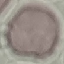

Malaria status: uninfected. Cell patch, automatically extracted from a larger field of view and resized to 64 × 64 pixels. Acquired by smartphone through the microscope eyepiece. Giemsa-stained preparation. Thin blood film.